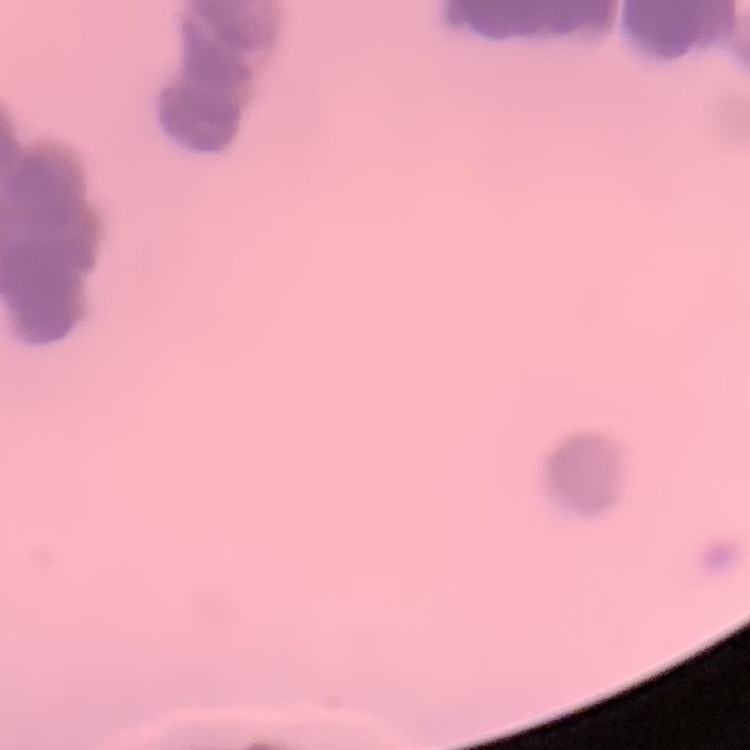

red_blood_cell_morphology: rouleaux formation
preparation: thin blood film
stain: Field's or Giemsa
image_type: one tile cut from a larger photomicrograph